Point out each leukocyte.
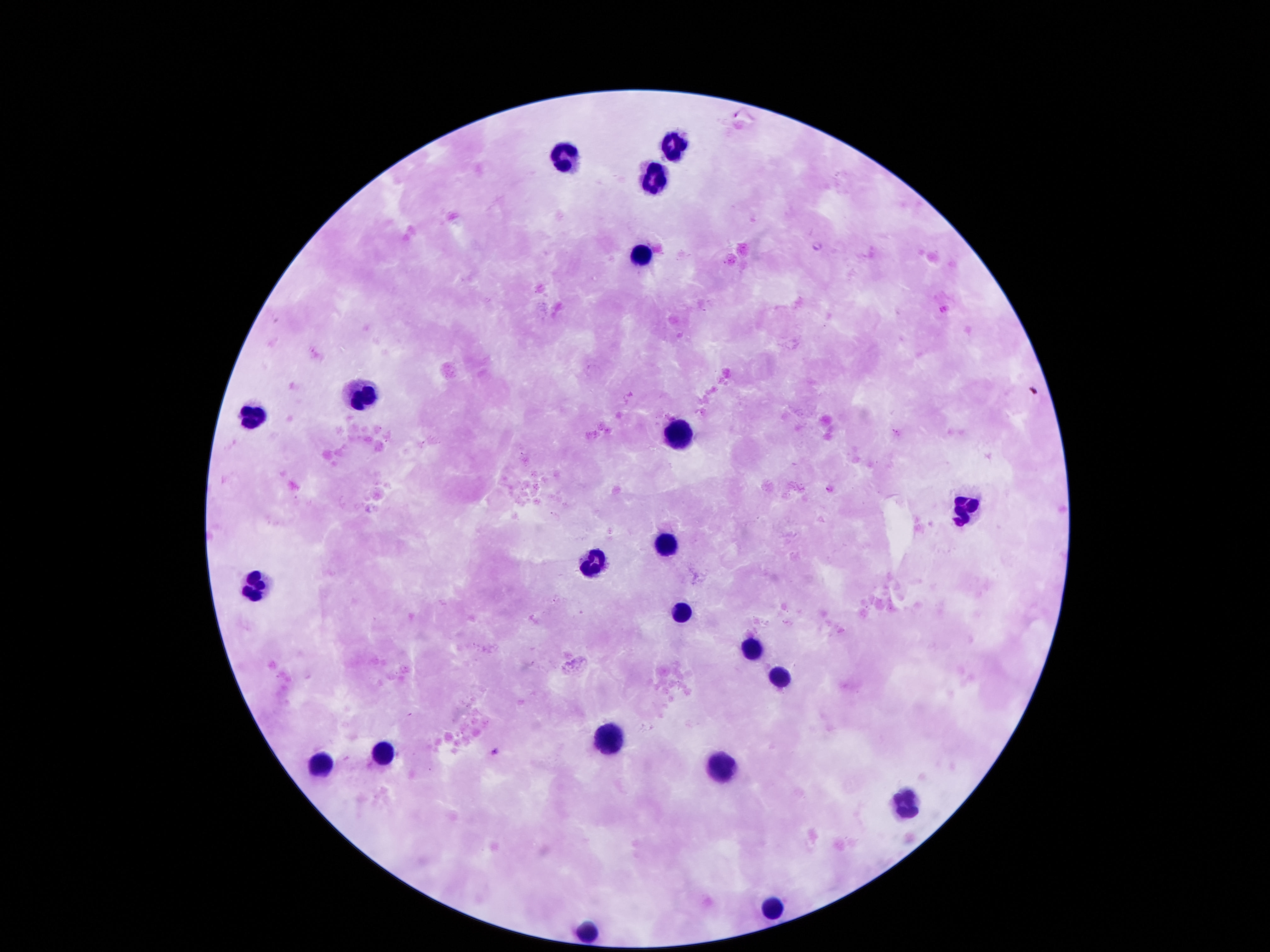

Approximate centers as {x, y} in pixels.
Leukocytes: {671, 140}, {563, 154}, {651, 177}, {641, 251}, {362, 388}, {248, 416}, {674, 432}, {967, 507}, {661, 541}, {590, 564}, {254, 584}, {681, 611}, {748, 647}, {775, 677}, {604, 734}, {385, 755}, {318, 759}, {725, 768}, {906, 802}, {772, 907}, {587, 927}.

preparation = thick blood smear
stain = Giemsa
image size = 1270×952 pixels
patient malaria status = uninfected
magnification = 100x
field of view = single
capture = smartphone camera through the microscope eyepiece